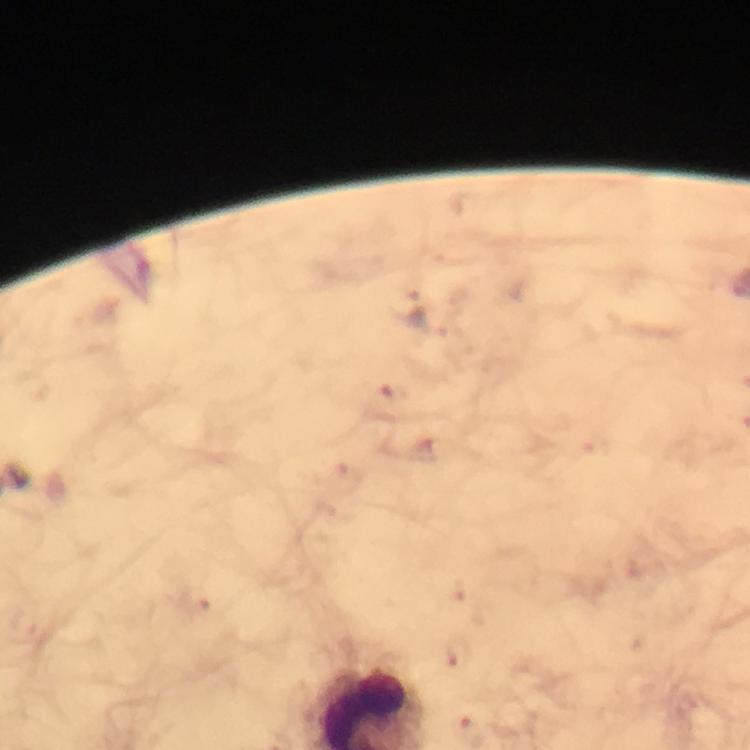
capture = smartphone photograph through a microscope
Plasmodium parasite locations = approximate object centers, in pixels from the top-left corner: (x=392, y=392), (x=197, y=601), (x=462, y=656)
context = from a diagnostic examination for malaria
cropped from = one field of view
immersion oil = applied
image size = 750×750 pixels
magnification = 100x
preparation = thick blood film
stain = Giemsa